Give the position of each Plasmodium falciparum parasite with its life-cycle stage, each leukocyte, and any debris.
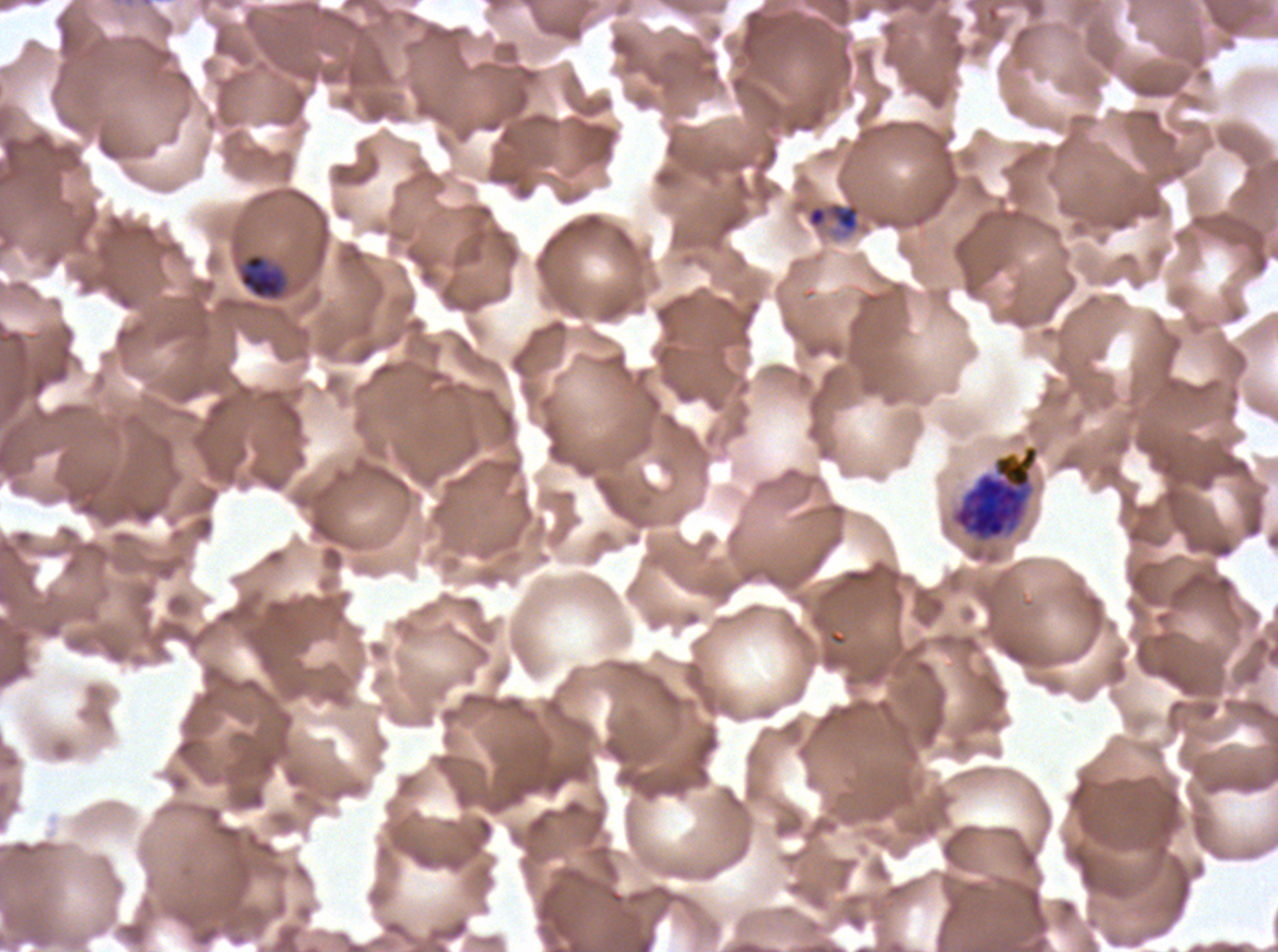

Approximate bounding boxes as [x1, y1, x2, y2] in pixels.
Rings: [805, 201, 861, 235].
Mid trophozoites: [239, 253, 286, 299].
Early schizonts: [951, 444, 1039, 543].
No late-ring/early-trophozoite forms, late trophozoites, late schizonts, segmenters, gametocytes, leukocytes, or debris observed.

stain = Giemsa
field of view = one sub-image of a larger composite
life-cycle stages observed = ring, mid trophozoite, early schizont
image size = 1278×952 pixels
specimen = Plasmodium falciparum from a patient in The Gambia, cultured ex vivo for 24 to 48 hours
preparation = thin blood film